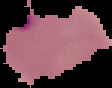
Summary:
  - Result: Plasmodium parasites identified
  - Image type: segmented cell region on a black background
  - Preparation: thin blood smear
  - Image size: 112×88 pixels